Outline each blood parasite and name the species.
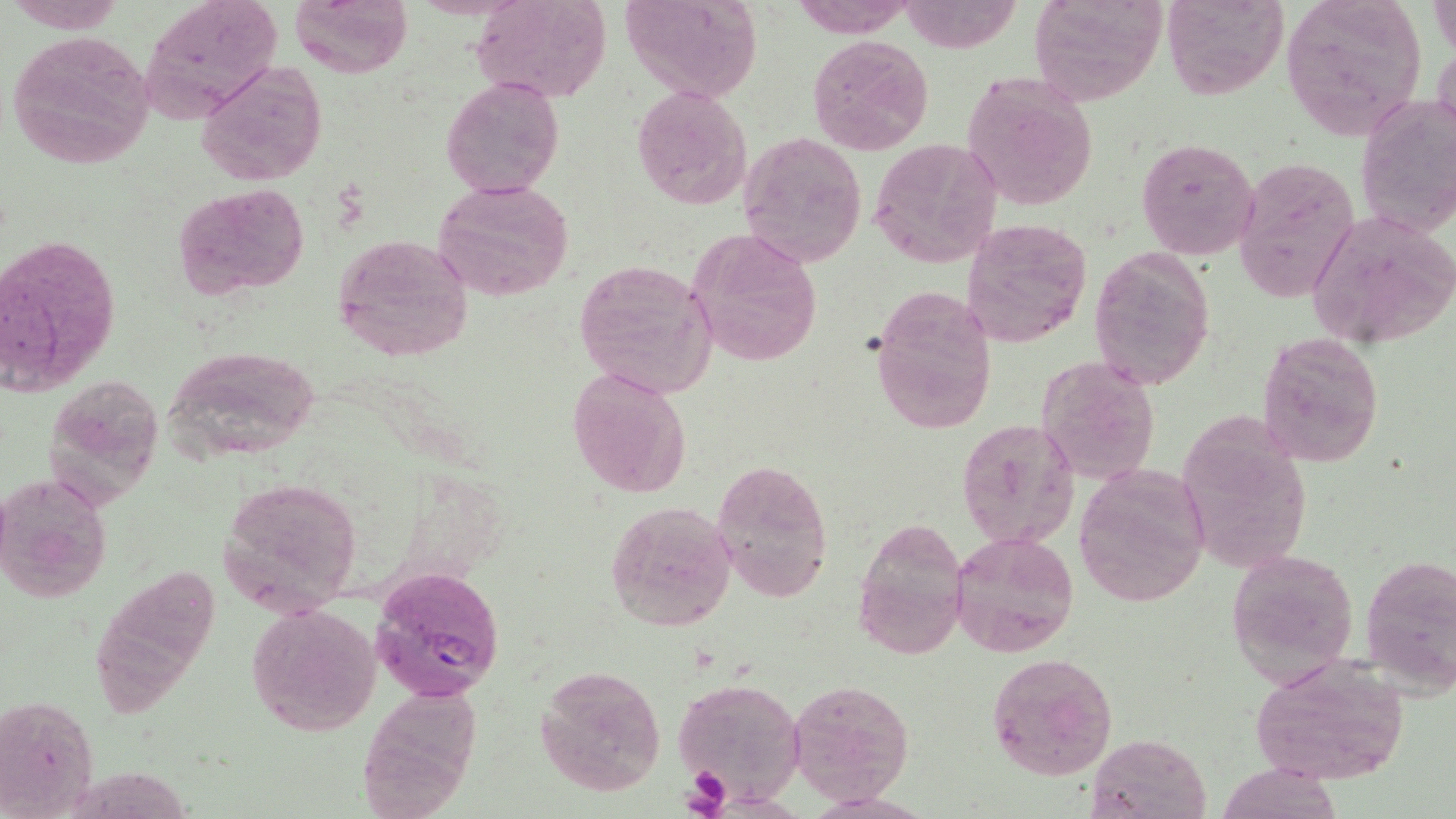

Approximate bounding boxes as [x1, y1, x2, y2] in pixels.
Plasmodium falciparum-infected red blood cells: [372, 566, 503, 700].
No Plasmodium ovale, Plasmodium malariae, Plasmodium vivax, Babesia divergens, or Trypanosoma brucei observed.

slide_level_diagnosis: Plasmodium falciparum
platelet_locations: 'approximate bounding boxes as [x1, y1, x2, y2] in pixels: [682, 770, 731, 814]'
field_of_view: one of a larger specimen
image_size: 1456×819 pixels
uninfected_red_blood_cell_locations: 'approximate bounding boxes as [x1, y1, x2, y2] in pixels: [8, 0, 125, 32], [139, 0, 281, 118], [288, 0, 413, 77], [470, 0, 613, 103], [617, 0, 762, 106], [788, 0, 919, 38], [899, 0, 1022, 53], [1029, 0, 1167, 107], [1163, 0, 1288, 99], [1280, 0, 1430, 138], [1429, 4, 1455, 57], [6, 29, 157, 169], [807, 33, 933, 156], [1433, 35, 1456, 154], [196, 61, 328, 186], [962, 71, 1099, 211], [440, 77, 565, 200], [631, 84, 753, 212], [1355, 92, 1454, 240], [738, 131, 869, 268], [1136, 137, 1259, 260], [868, 139, 1004, 270], [1234, 156, 1361, 303], [433, 178, 574, 301], [173, 182, 310, 298], [1304, 212, 1456, 350], [961, 215, 1093, 349], [687, 227, 823, 368], [5, 234, 120, 398], [331, 234, 475, 364], [1088, 247, 1216, 390], [574, 259, 717, 399], [869, 287, 997, 436], [1257, 331, 1386, 466], [160, 344, 323, 463], [1035, 356, 1160, 486], [567, 366, 691, 499], [46, 373, 162, 503], [1173, 413, 1312, 580], [955, 418, 1080, 550], [713, 458, 834, 604], [1075, 465, 1212, 606], [0, 473, 111, 604], [218, 477, 364, 614], [605, 499, 737, 633], [852, 514, 968, 660], [949, 529, 1080, 659], [1227, 548, 1358, 683], [1360, 552, 1456, 695], [246, 603, 381, 737], [984, 653, 1118, 781], [1249, 661, 1409, 785], [535, 664, 666, 798], [673, 677, 803, 803], [788, 679, 913, 804], [0, 695, 100, 817], [1087, 732, 1209, 817], [1214, 762, 1345, 818]'
modality: light microscopy
stain: May-Grünwald-Giemsa
magnification: 1000x
preparation: thin blood film